Assess this cell for malaria.
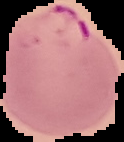

It is parasitized.

preparation = thin blood smear
image type = segmented cell region on a black background
image size = 124×142 pixels